Assess this cell for malaria.
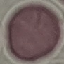
Uninfected.

Summary:
  - Image type: automatically extracted cell patch, resized to 64 × 64 pixels
  - Stain: Giemsa
  - Preparation: thin blood film
  - Capture: smartphone camera at the microscope eyepiece